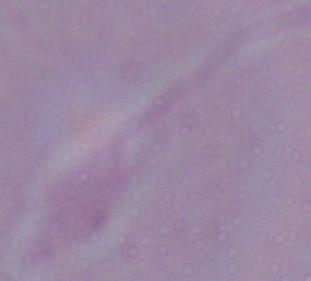
Summary:
  - Modality: micrograph
  - Identification: Leishmania
  - Magnification: 1000x